State the preparation type.
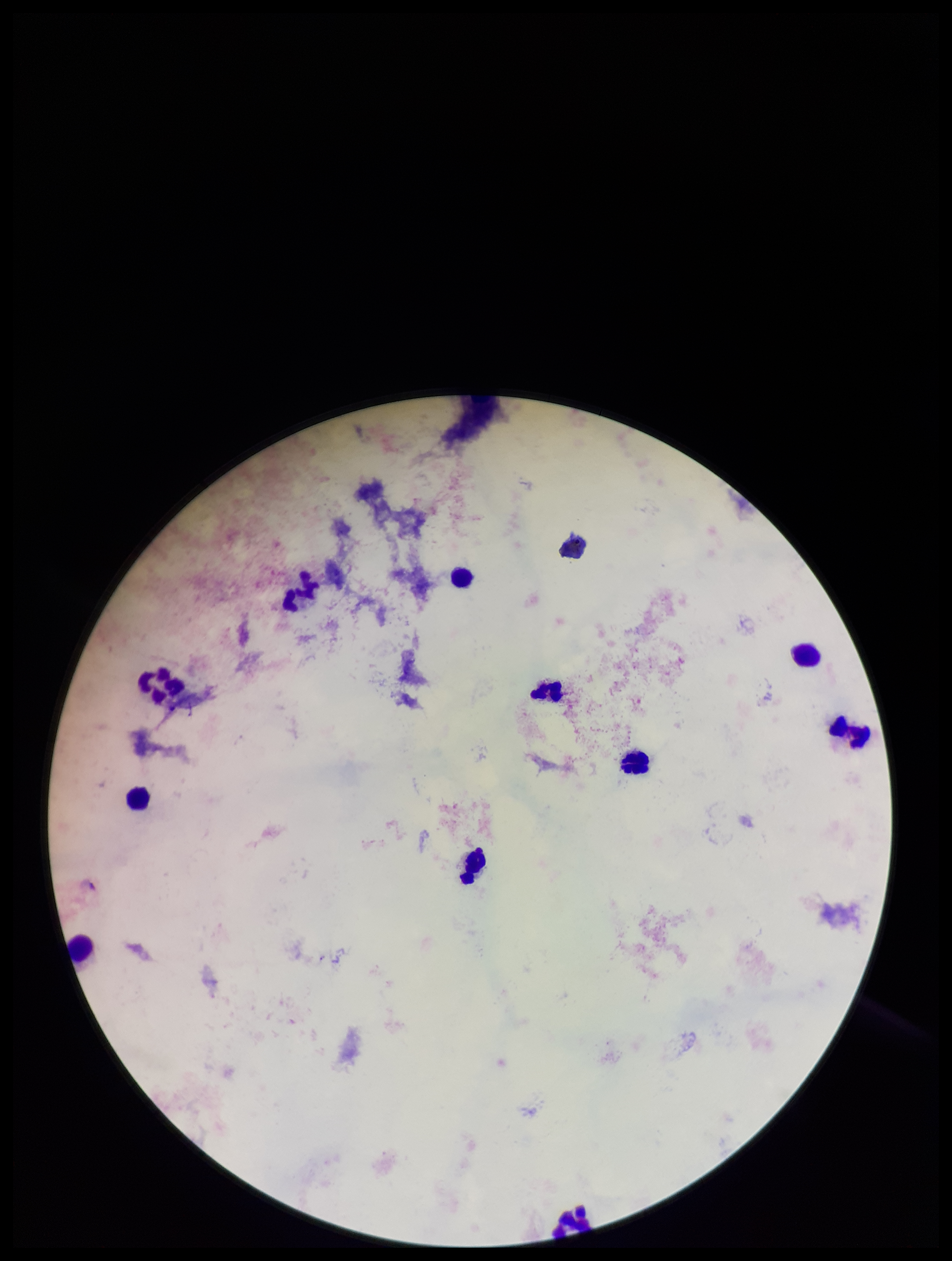

Thick.

Summary:
  - Field of view: single
  - Parasite count: 0
  - Plasmodium parasites: none identified
  - Patient malaria status: negative
  - Stain: Giemsa
  - Image size: 952×1261 pixels
  - Capture: smartphone photograph through the microscope eyepiece
  - Leukocyte count: 12